Give the position of every malaria parasite.
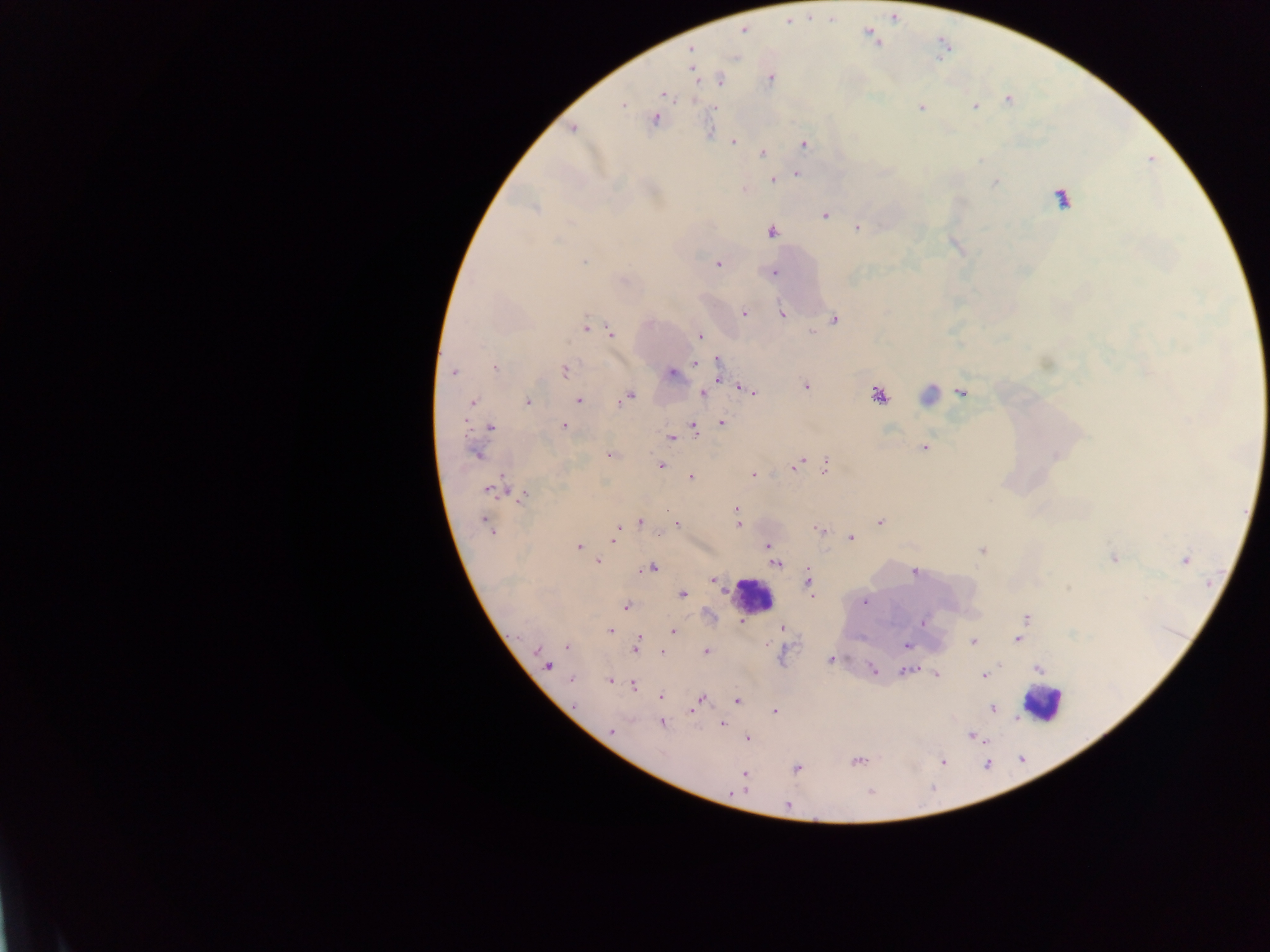
Approximate centers as {x, y} in pixels.
Malaria parasites: {743, 31}, {692, 50}, {770, 78}, {720, 80}, {663, 95}, {1007, 100}, {622, 104}, {975, 107}, {921, 108}, {654, 119}, {572, 128}, {733, 142}, {804, 144}, {762, 153}, {797, 174}, {771, 181}, {995, 183}, {744, 190}, {1062, 198}, {534, 208}, {824, 216}, {857, 228}, {771, 232}, {584, 261}, {718, 263}, {773, 272}, {744, 313}, {782, 314}, {834, 320}, {585, 327}, {611, 333}, {700, 336}, {718, 362}, {695, 363}, {495, 368}, {565, 371}, {453, 372}, {671, 373}, {719, 377}, {806, 385}, {747, 390}, {962, 392}, {704, 394}, {929, 395}, {878, 396}, {628, 397}, {578, 401}, {624, 401}, {527, 402}, {472, 403}, {722, 422}, {564, 426}, {490, 427}, {694, 429}, {672, 437}, {924, 447}, {475, 454}, {609, 455}, {660, 466}, {794, 466}, {825, 466}, {754, 475}, {690, 478}, {489, 490}, {524, 495}, {737, 509}, {669, 511}, {640, 522}, {880, 522}, {487, 523}, {677, 525}, {738, 525}, {490, 530}, {819, 530}, {615, 532}, {614, 538}, {851, 538}, {768, 545}, {579, 546}, {982, 551}, {1114, 558}, {1185, 560}, {598, 561}, {776, 564}, {651, 568}, {646, 570}, {914, 573}, {807, 580}, {713, 581}, {683, 594}, {864, 602}, {626, 606}, {1026, 618}, {923, 622}, {782, 627}, {611, 631}, {673, 631}, {638, 639}, {1018, 639}, {973, 642}, {907, 645}, {567, 647}, {636, 649}, {706, 651}, {663, 653}, {831, 659}, {547, 665}, {1038, 668}, {873, 669}, {906, 671}, {936, 674}, {984, 675}, {571, 679}, {609, 682}, {633, 685}, {661, 696}, {701, 699}, {737, 700}, {696, 705}, {992, 708}, {693, 711}, {774, 711}, {662, 723}, {722, 724}, {611, 730}, {972, 735}, {748, 739}, {856, 762}, {943, 762}, {797, 768}, {744, 774}, {869, 793}, {787, 805}.

Leukocyte locations: {751, 596}, {1043, 703}. Sample from Ghana. Photographed through a microscope with a mobile-phone camera. One field of view. Thick blood film. Image is 1270×952 pixels.